Classify this cell by malaria status.
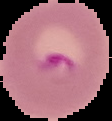

Parasitized.

Summary:
  - Image type: segmented cell region with the area outside set to black
  - Preparation: thin blood smear
  - Image size: 112×121 pixels